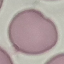
malaria status = uninfected
preparation = thin smear
capture = smartphone camera at the microscope eyepiece
image type = automatically extracted cell patch, resized to 64 × 64 pixels
stain = Giemsa